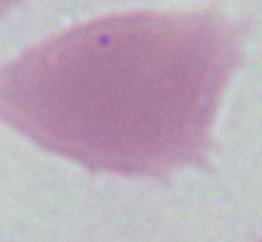 An erythrocyte is shown. 1000x magnification. Micrograph.